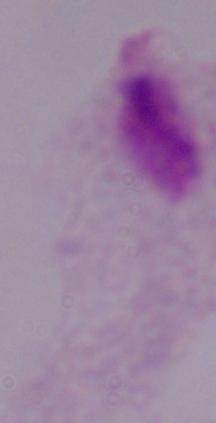

Micrograph. A trichomonad is seen. 1000x magnification.